Locate Plasmodium parasites and leukocytes.
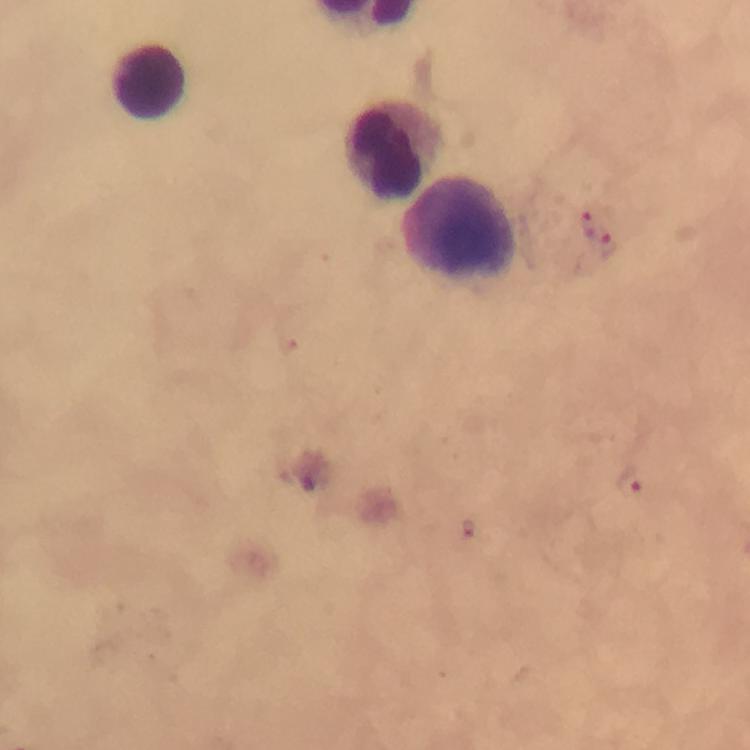
Approximate centers as [x, y] in pixels.
Plasmodium parasites: [588, 223], [609, 247], [632, 483], [469, 528].
Leukocytes: [148, 83], [397, 150], [458, 228].

context: from a malaria diagnostic workup
magnification: 100x
image_size: 750×750 pixels
immersion_oil: applied
preparation: thick smear
stain: Giemsa
capture: smartphone camera through the microscope
cropped_from: one field of view